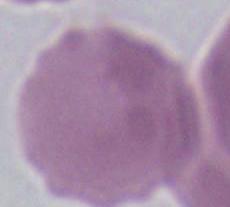

Summary:
  - Modality: photomicrograph
  - Magnification: 1000x
  - Identification: red blood cell